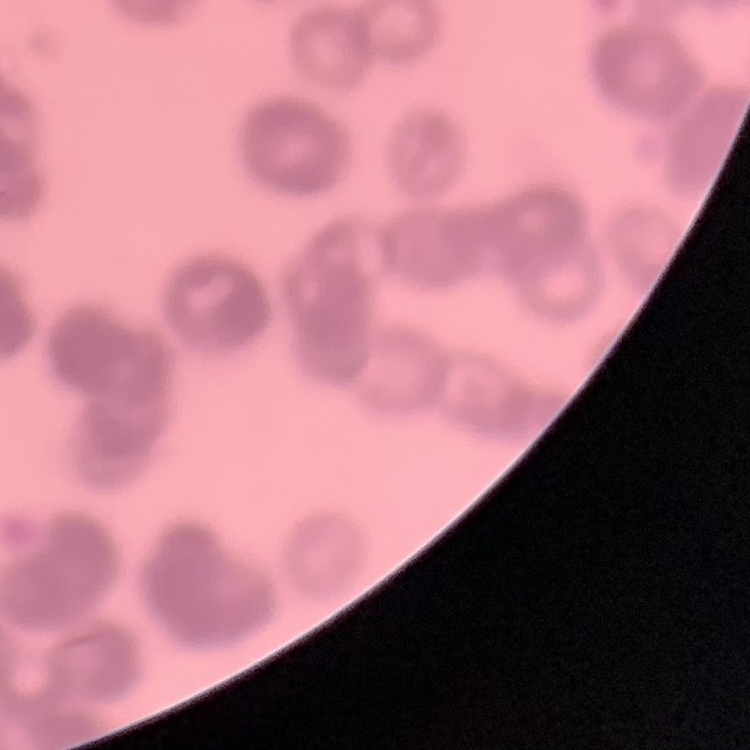

The erythrocytes exhibit rouleaux formation. Thin peripheral smear. One tile cut from a larger photomicrograph. Field's or Giemsa stain.